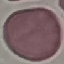
Summary:
  - Malaria status: uninfected
  - Stain: Giemsa
  - Capture: smartphone through the microscope eyepiece
  - Image type: automatically extracted cell patch, resized to 64 × 64 pixels
  - Preparation: thin blood film